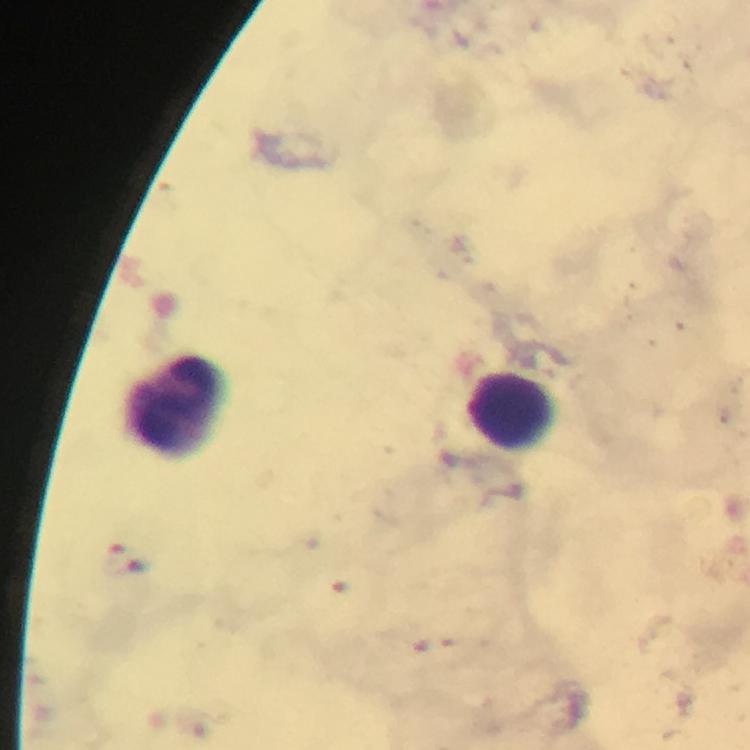
Approximate centers as [x, y] in pixels.
Summary:
  - Leukocyte locations: [177, 408], [512, 409]
  - Preparation: thick smear
  - Stain: Giemsa
  - Context: from a malaria diagnostic workup
  - Cropped from: a single field of view
  - Capture: smartphone photograph through a microscope
  - Immersion oil: used
  - Plasmodium parasites: none detected
  - Image size: 750×750 pixels
  - Magnification: 100x